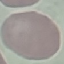
malaria status = uninfected
stain = Giemsa
capture = smartphone through the microscope eyepiece
preparation = thin blood smear
image type = automatically extracted cell patch, resized to 64 × 64 pixels